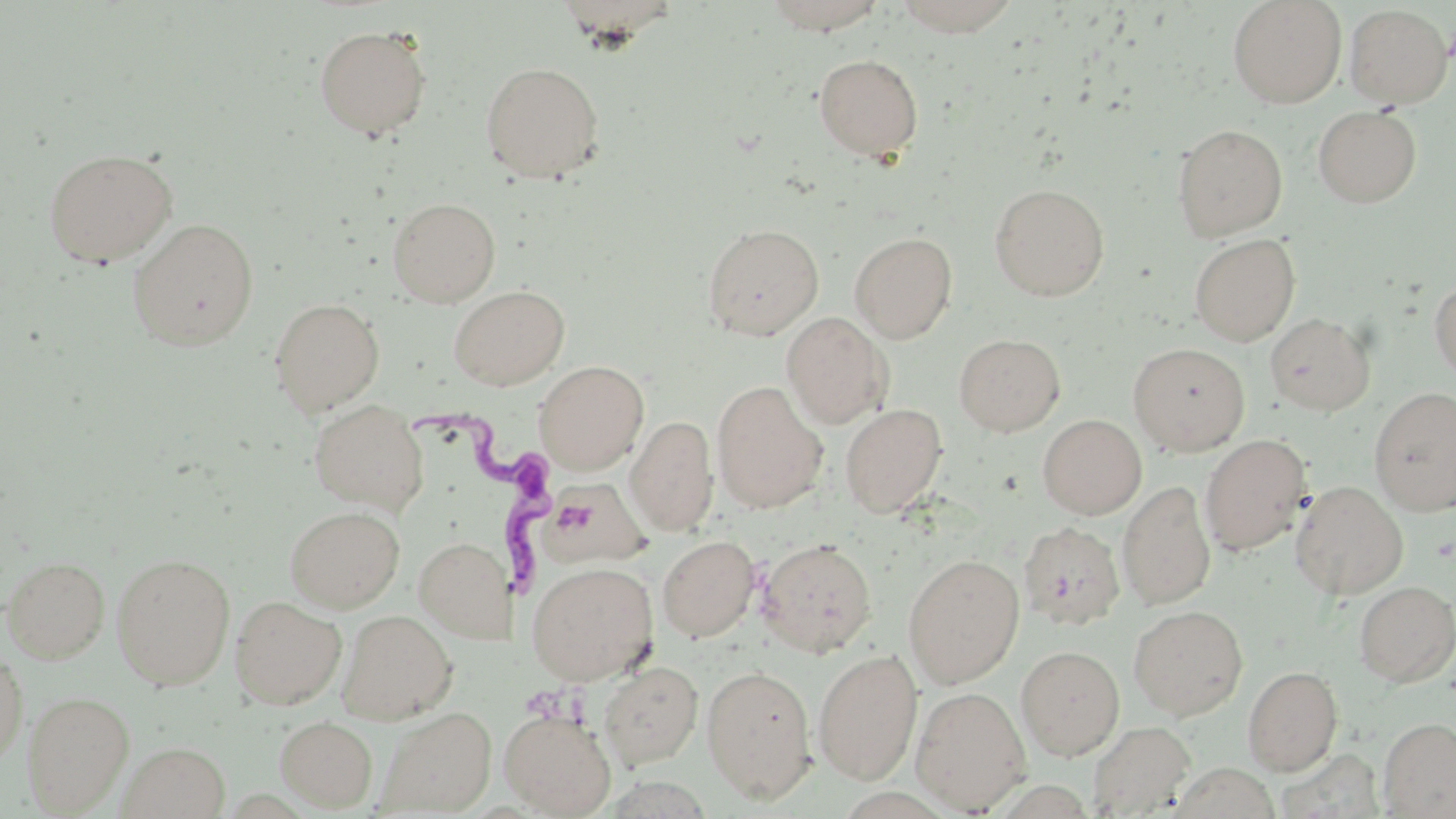

Approximate bounding boxes as named x1/y1/x2/y2 corners in pixels. Trypanosoma brucei locations: (x1=409, y1=404, x2=555, y2=613). Uninfected red blood cell locations: (x1=760, y1=0, x2=891, y2=34), (x1=892, y1=0, x2=1023, y2=36), (x1=1227, y1=0, x2=1347, y2=108), (x1=1343, y1=4, x2=1452, y2=109), (x1=314, y1=24, x2=432, y2=140), (x1=814, y1=53, x2=924, y2=161), (x1=481, y1=61, x2=604, y2=182), (x1=1313, y1=106, x2=1421, y2=208), (x1=1172, y1=123, x2=1288, y2=240), (x1=43, y1=147, x2=178, y2=267), (x1=989, y1=183, x2=1110, y2=301), (x1=387, y1=197, x2=501, y2=307), (x1=127, y1=217, x2=260, y2=351), (x1=702, y1=222, x2=824, y2=339), (x1=849, y1=232, x2=958, y2=343), (x1=1189, y1=233, x2=1300, y2=346), (x1=1429, y1=277, x2=1456, y2=384), (x1=448, y1=284, x2=571, y2=390), (x1=269, y1=297, x2=385, y2=415), (x1=781, y1=311, x2=894, y2=429), (x1=1264, y1=313, x2=1376, y2=415), (x1=953, y1=333, x2=1065, y2=436), (x1=1128, y1=342, x2=1250, y2=456), (x1=534, y1=360, x2=649, y2=474), (x1=712, y1=380, x2=828, y2=513), (x1=1369, y1=387, x2=1456, y2=514), (x1=308, y1=399, x2=428, y2=513), (x1=840, y1=403, x2=948, y2=517), (x1=1038, y1=414, x2=1147, y2=519), (x1=626, y1=415, x2=718, y2=534), (x1=1200, y1=434, x2=1312, y2=557), (x1=542, y1=477, x2=649, y2=568), (x1=1290, y1=480, x2=1409, y2=600), (x1=1117, y1=481, x2=1216, y2=610), (x1=284, y1=505, x2=404, y2=612), (x1=1018, y1=522, x2=1126, y2=631), (x1=657, y1=535, x2=760, y2=642), (x1=414, y1=536, x2=513, y2=643), (x1=758, y1=538, x2=877, y2=657), (x1=111, y1=553, x2=235, y2=690), (x1=903, y1=554, x2=1025, y2=688), (x1=2, y1=556, x2=110, y2=663), (x1=527, y1=561, x2=658, y2=685), (x1=1354, y1=580, x2=1456, y2=687), (x1=230, y1=595, x2=347, y2=709), (x1=1128, y1=605, x2=1248, y2=720), (x1=338, y1=610, x2=457, y2=724), (x1=0, y1=641, x2=27, y2=768), (x1=1016, y1=645, x2=1125, y2=760), (x1=813, y1=648, x2=923, y2=785), (x1=598, y1=662, x2=704, y2=769), (x1=701, y1=664, x2=818, y2=802), (x1=1243, y1=665, x2=1343, y2=775), (x1=910, y1=685, x2=1031, y2=814), (x1=23, y1=690, x2=134, y2=814), (x1=375, y1=706, x2=496, y2=816), (x1=499, y1=708, x2=617, y2=817), (x1=274, y1=716, x2=378, y2=811), (x1=1378, y1=718, x2=1456, y2=818), (x1=1087, y1=720, x2=1196, y2=817), (x1=119, y1=742, x2=230, y2=818). Slide-level diagnosis: Trypanosoma brucei. Thin blood smear. May-Grünwald-Giemsa-stained preparation. 1000x magnification. Light microscopy. Image is 1456×819 pixels. Single field of view.